Outline each blood parasite and name the species.
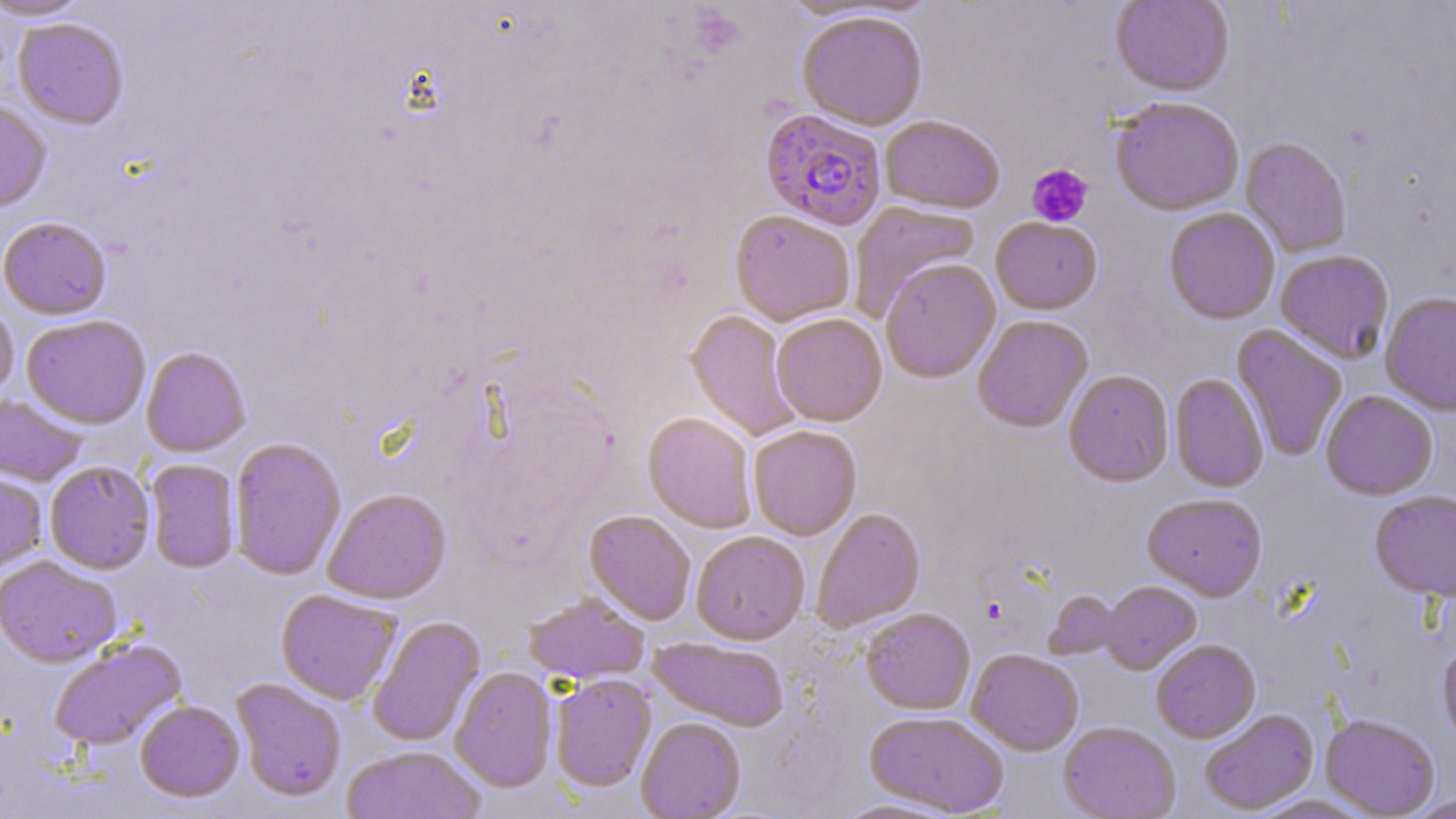

Approximate bounding boxes as named x1/y1/x2/y2 corners in pixels.
Plasmodium falciparum-infected red blood cells: (x1=760, y1=109, x2=887, y2=230).
No Plasmodium ovale, Plasmodium malariae, Plasmodium vivax, Babesia divergens, or Trypanosoma brucei observed.

Uninfected red blood cell locations: (x1=0, y1=0, x2=92, y2=21), (x1=1110, y1=0, x2=1234, y2=98), (x1=797, y1=10, x2=928, y2=130), (x1=13, y1=19, x2=129, y2=131), (x1=1109, y1=99, x2=1245, y2=217), (x1=0, y1=102, x2=51, y2=215), (x1=880, y1=115, x2=1005, y2=214), (x1=1240, y1=137, x2=1351, y2=258), (x1=849, y1=201, x2=982, y2=321), (x1=1164, y1=207, x2=1280, y2=325), (x1=730, y1=210, x2=855, y2=326), (x1=0, y1=217, x2=112, y2=321), (x1=991, y1=218, x2=1102, y2=315), (x1=1275, y1=250, x2=1394, y2=365), (x1=880, y1=259, x2=1000, y2=383), (x1=1252, y1=259, x2=1367, y2=415), (x1=1380, y1=292, x2=1456, y2=416), (x1=0, y1=293, x2=19, y2=406), (x1=685, y1=309, x2=803, y2=442), (x1=772, y1=313, x2=887, y2=426), (x1=21, y1=315, x2=151, y2=429), (x1=972, y1=315, x2=1093, y2=433), (x1=1232, y1=325, x2=1348, y2=462), (x1=141, y1=347, x2=250, y2=457), (x1=1064, y1=370, x2=1174, y2=487), (x1=1170, y1=373, x2=1268, y2=493), (x1=1320, y1=390, x2=1438, y2=500), (x1=0, y1=394, x2=85, y2=487), (x1=643, y1=412, x2=757, y2=533), (x1=748, y1=424, x2=862, y2=540), (x1=229, y1=438, x2=346, y2=580), (x1=146, y1=459, x2=240, y2=574), (x1=45, y1=462, x2=155, y2=575), (x1=0, y1=468, x2=48, y2=577), (x1=322, y1=488, x2=451, y2=604), (x1=1369, y1=491, x2=1456, y2=603), (x1=1142, y1=494, x2=1267, y2=601), (x1=810, y1=508, x2=925, y2=633), (x1=584, y1=510, x2=696, y2=625), (x1=691, y1=530, x2=810, y2=644), (x1=0, y1=556, x2=122, y2=668), (x1=1099, y1=581, x2=1201, y2=674), (x1=276, y1=589, x2=401, y2=705), (x1=1044, y1=590, x2=1125, y2=660), (x1=524, y1=593, x2=649, y2=684), (x1=861, y1=608, x2=975, y2=714), (x1=367, y1=615, x2=486, y2=748), (x1=649, y1=637, x2=788, y2=731), (x1=48, y1=638, x2=187, y2=751), (x1=1151, y1=638, x2=1261, y2=743), (x1=1438, y1=641, x2=1456, y2=753), (x1=967, y1=649, x2=1083, y2=756), (x1=450, y1=667, x2=558, y2=792), (x1=550, y1=674, x2=656, y2=792), (x1=231, y1=678, x2=346, y2=803), (x1=135, y1=701, x2=244, y2=802), (x1=1199, y1=708, x2=1319, y2=815), (x1=865, y1=712, x2=1009, y2=817), (x1=1320, y1=715, x2=1441, y2=818), (x1=636, y1=717, x2=746, y2=818), (x1=1058, y1=722, x2=1180, y2=819), (x1=340, y1=746, x2=486, y2=819), (x1=1406, y1=794, x2=1456, y2=817), (x1=1249, y1=795, x2=1375, y2=818), (x1=831, y1=797, x2=967, y2=818). Platelet locations: (x1=1027, y1=164, x2=1093, y2=227), (x1=980, y1=597, x2=1008, y2=624). Slide-level diagnosis: Plasmodium falciparum. Captured at 1000x magnification. Single field of view. Image is 1456×819 pixels. May-Grünwald-Giemsa-stained preparation. Light microscopy. Thin blood film.